Point out each malaria parasite.
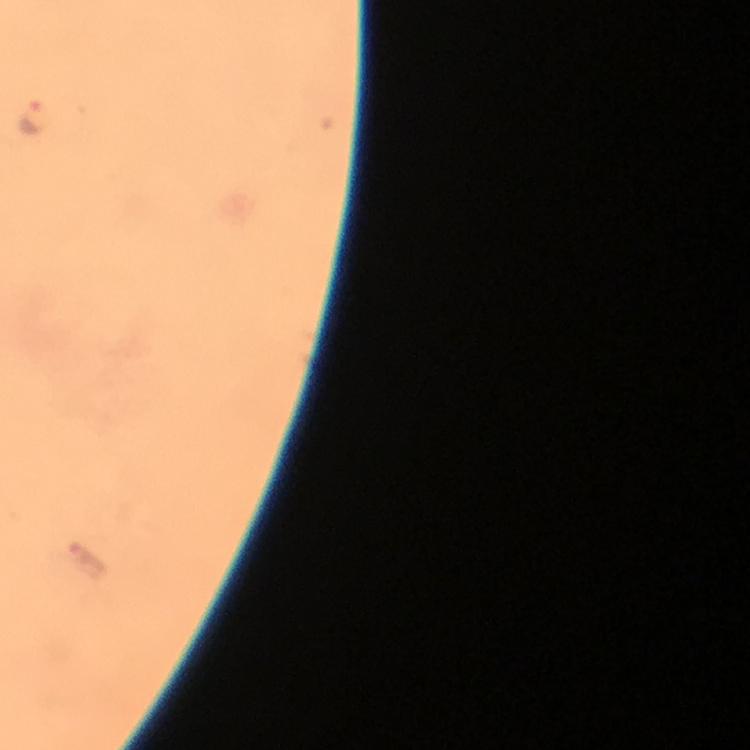

Approximate centers as {x, y} in pixels.
Malaria parasites: {33, 119}, {88, 560}.

Immersion oil applied. A crop from one field of view. Thick blood smear. At 100x magnification. Image is 750×750 pixels. Smartphone photograph taken through a microscope. Giemsa stain. From a malaria diagnostic workup.